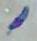

Summary:
  - Modality: photomicrograph
  - Magnification: 1000x
  - Identification: Toxoplasma gondii